Locate and identify every blood parasite.
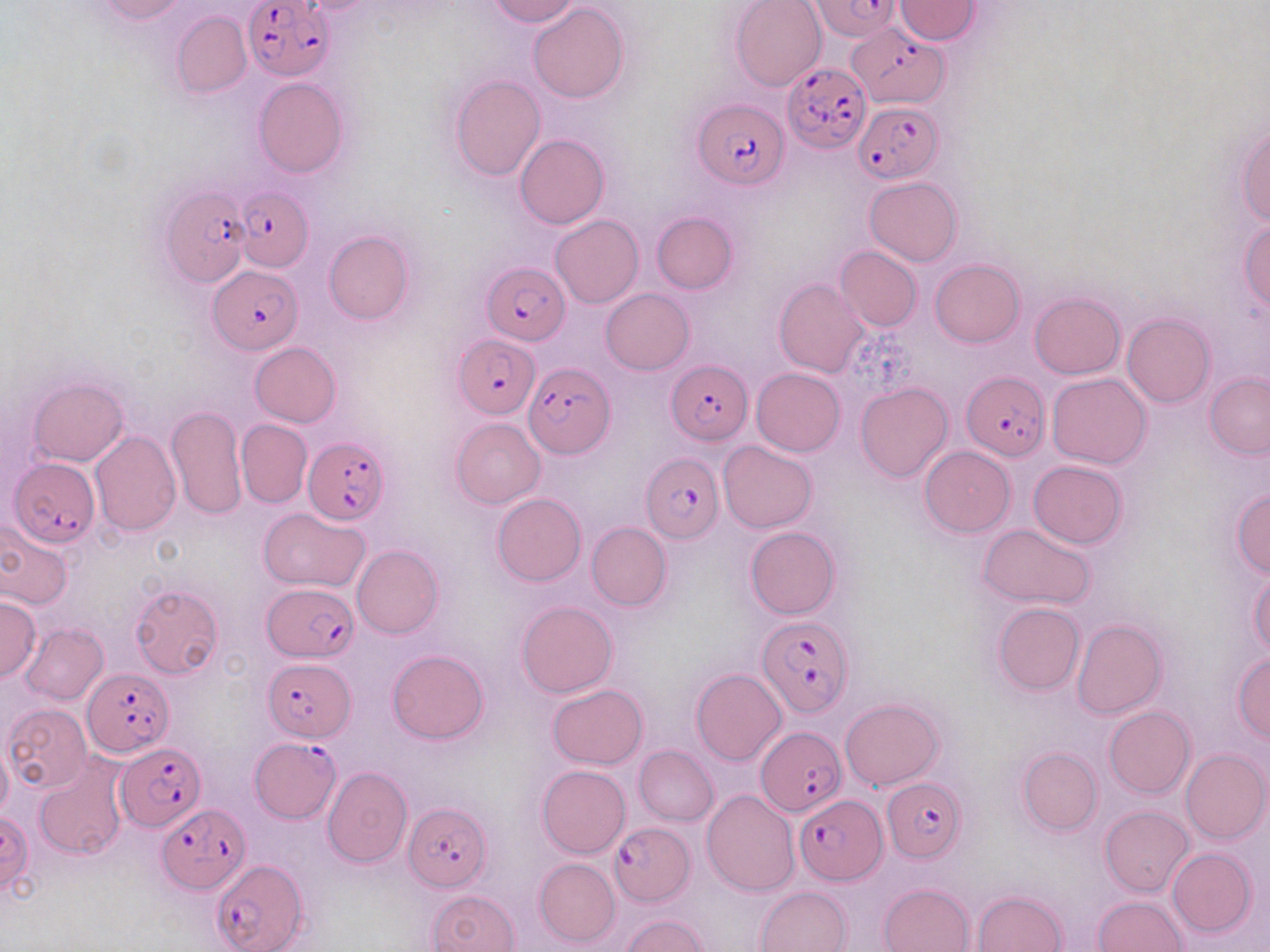

Approximate bounding boxes as [x1, y1, x2, y2] in pixels.
Plasmodium falciparum-infected red blood cells: [244, 0, 334, 81], [809, 0, 903, 41], [853, 22, 949, 109], [781, 61, 873, 154], [692, 98, 789, 189], [853, 101, 943, 182], [161, 182, 251, 290], [234, 187, 312, 273], [483, 260, 567, 344], [209, 266, 302, 353], [453, 334, 539, 416], [667, 359, 753, 444], [522, 361, 614, 457], [963, 373, 1048, 462], [304, 437, 391, 523], [642, 454, 723, 543], [8, 459, 97, 546], [263, 583, 359, 662], [758, 616, 854, 717], [263, 658, 356, 740], [82, 669, 172, 758], [756, 724, 847, 821], [249, 737, 339, 821], [116, 742, 204, 829], [885, 778, 966, 864], [794, 794, 886, 885], [405, 803, 491, 891], [156, 805, 249, 892], [607, 822, 694, 906], [212, 861, 306, 952].
No Plasmodium ovale, Plasmodium malariae, Plasmodium vivax, Babesia divergens, or Trypanosoma brucei observed.

Uninfected red blood cell locations: [95, 0, 187, 23], [488, 0, 580, 26], [730, 0, 827, 90], [895, 0, 980, 43], [528, 3, 627, 103], [173, 11, 251, 98], [450, 74, 544, 182], [253, 77, 348, 176], [1236, 122, 1269, 228], [515, 134, 608, 229], [864, 177, 962, 265], [652, 211, 737, 294], [551, 214, 644, 307], [1239, 219, 1269, 313], [323, 231, 414, 324], [834, 246, 921, 332], [931, 259, 1024, 347], [774, 278, 869, 378], [601, 288, 694, 374], [1030, 292, 1124, 378], [1122, 312, 1215, 408], [250, 342, 341, 428], [751, 368, 845, 456], [1204, 372, 1270, 458], [1046, 373, 1153, 468], [29, 378, 128, 466], [856, 382, 953, 482], [166, 404, 247, 520], [451, 418, 545, 508], [236, 420, 313, 508], [90, 430, 180, 536], [730, 439, 825, 618], [719, 440, 816, 533], [920, 446, 1015, 536], [1028, 460, 1128, 548], [1230, 488, 1270, 576], [492, 493, 586, 585], [257, 507, 369, 592], [0, 519, 74, 612], [586, 522, 672, 611], [979, 524, 1097, 609], [745, 528, 841, 618], [352, 545, 443, 638], [1248, 566, 1269, 659], [129, 584, 223, 678], [0, 596, 40, 682], [517, 599, 618, 697], [992, 602, 1084, 695], [1072, 618, 1166, 720], [19, 623, 107, 704], [387, 649, 489, 743], [1231, 653, 1270, 742], [691, 669, 786, 765], [548, 684, 647, 768], [840, 697, 944, 789], [4, 704, 90, 792], [1105, 706, 1196, 798], [0, 742, 12, 818], [634, 745, 719, 826], [1017, 746, 1101, 836], [1180, 748, 1269, 844], [34, 759, 127, 860], [538, 765, 631, 858], [323, 767, 412, 868], [702, 789, 800, 897], [1100, 806, 1194, 897], [1167, 847, 1256, 938], [534, 858, 620, 947], [879, 883, 975, 952], [756, 886, 852, 952], [427, 890, 520, 952], [972, 890, 1069, 951], [1093, 895, 1186, 951], [621, 914, 709, 952]. Slide-level diagnosis: Plasmodium falciparum. Image is 1270×952 pixels. Captured at 1000x magnification. Thin blood smear. Single field of view. Light microscopy. May-Grünwald-Giemsa-stained preparation.